State the preparation type.
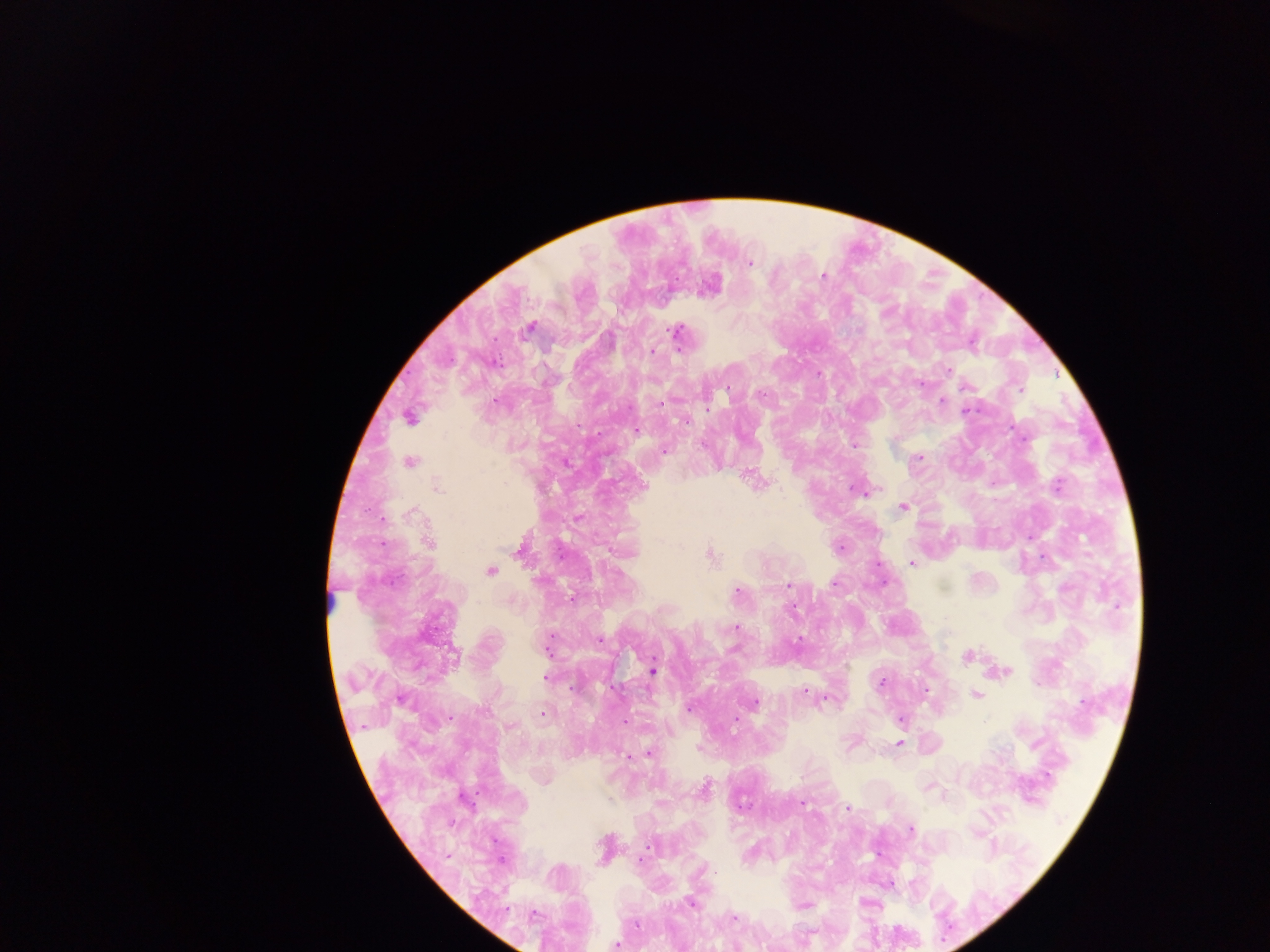

Thick blood smear.

malaria_parasite_locations: 'approximate centers as [x, y] in pixels: [750, 264], [823, 275], [676, 331], [495, 339], [680, 350], [655, 351], [499, 356], [502, 366], [947, 369], [924, 384], [967, 387], [727, 388], [1019, 390], [764, 394], [495, 400], [942, 401], [662, 404], [707, 409], [966, 409], [411, 416], [686, 423], [577, 426], [1011, 426], [638, 429], [599, 434], [854, 444], [664, 450], [917, 458], [1056, 485], [864, 496], [902, 506], [382, 518], [382, 545], [842, 546], [911, 563], [879, 565], [884, 581], [787, 583], [835, 583], [737, 592], [571, 600], [795, 606], [736, 627], [799, 640], [600, 641], [547, 652], [966, 656], [654, 671], [1005, 672], [544, 677], [882, 684], [612, 686], [924, 689], [803, 690], [975, 695], [827, 703], [755, 704], [689, 708], [544, 712], [451, 717], [622, 719], [737, 720], [361, 727], [510, 727], [899, 742], [647, 753], [627, 758], [477, 791], [460, 796], [803, 803], [474, 805], [742, 806], [846, 808], [909, 830], [495, 843], [641, 856], [504, 860], [690, 902], [536, 913], [734, 917], [616, 944]'
image_size: 1270×952 pixels
capture: mobile-phone photograph through a microscope
field_of_view: single
country: Ghana